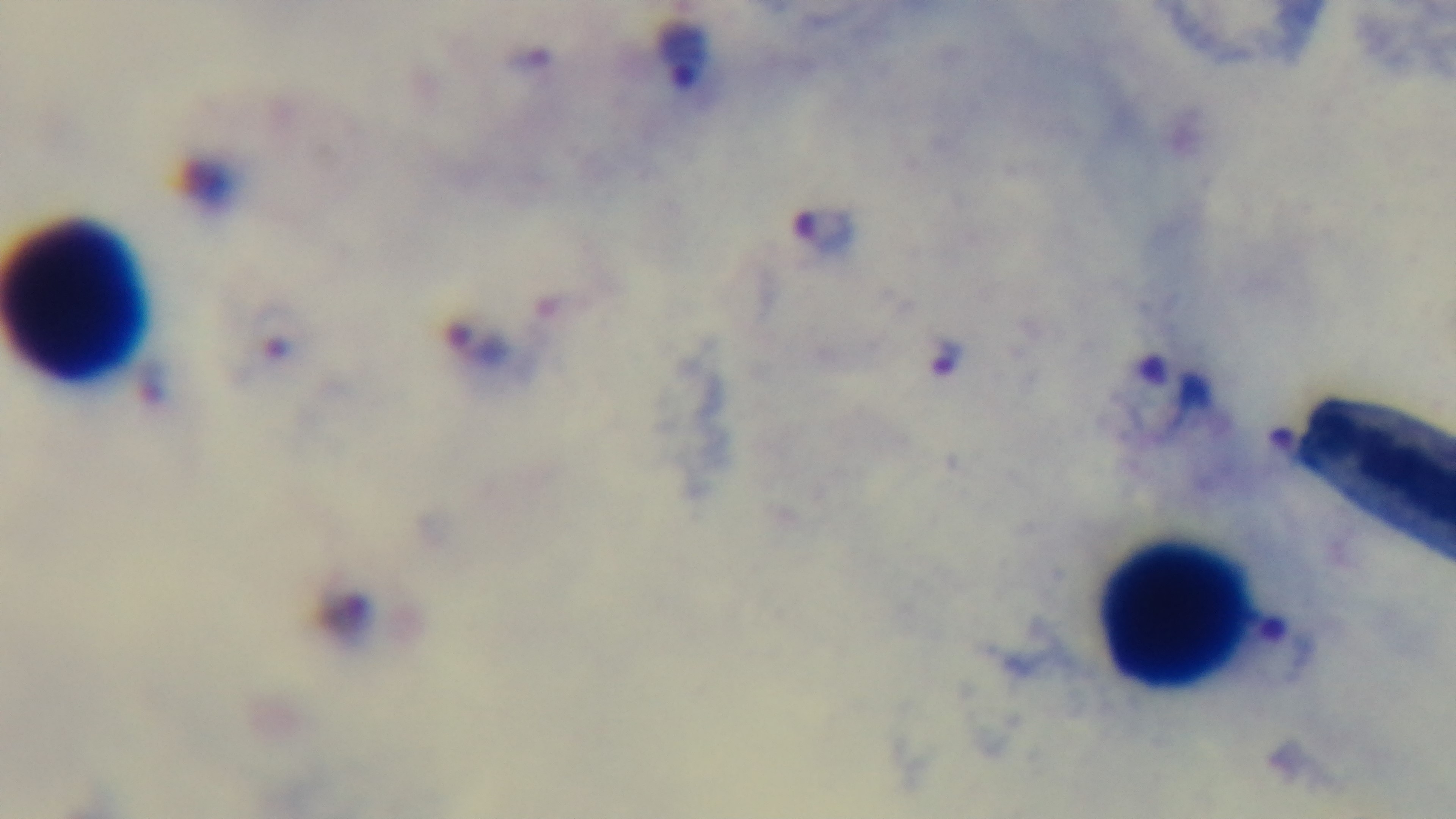
Summary:
  - Capture: mounted 4K digital camera
  - Modality: light microscopy
  - Stain: Giemsa
  - Field of view: single
  - Objective: 100x oil immersion
  - Malaria status: infected
  - Preparation: thick blood film